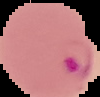
result = Plasmodium parasites detected
preparation = thin blood film
image type = cell region segmented out of the field of view; surrounding area masked to black
image size = 100×97 pixels